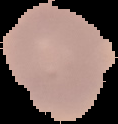

Summary:
  - Result: no malaria parasites seen
  - Image type: cell region segmented out of the field of view; surrounding area masked to black
  - Image size: 118×124 pixels
  - Preparation: thin blood film